Locate every blood parasite and identify its species.
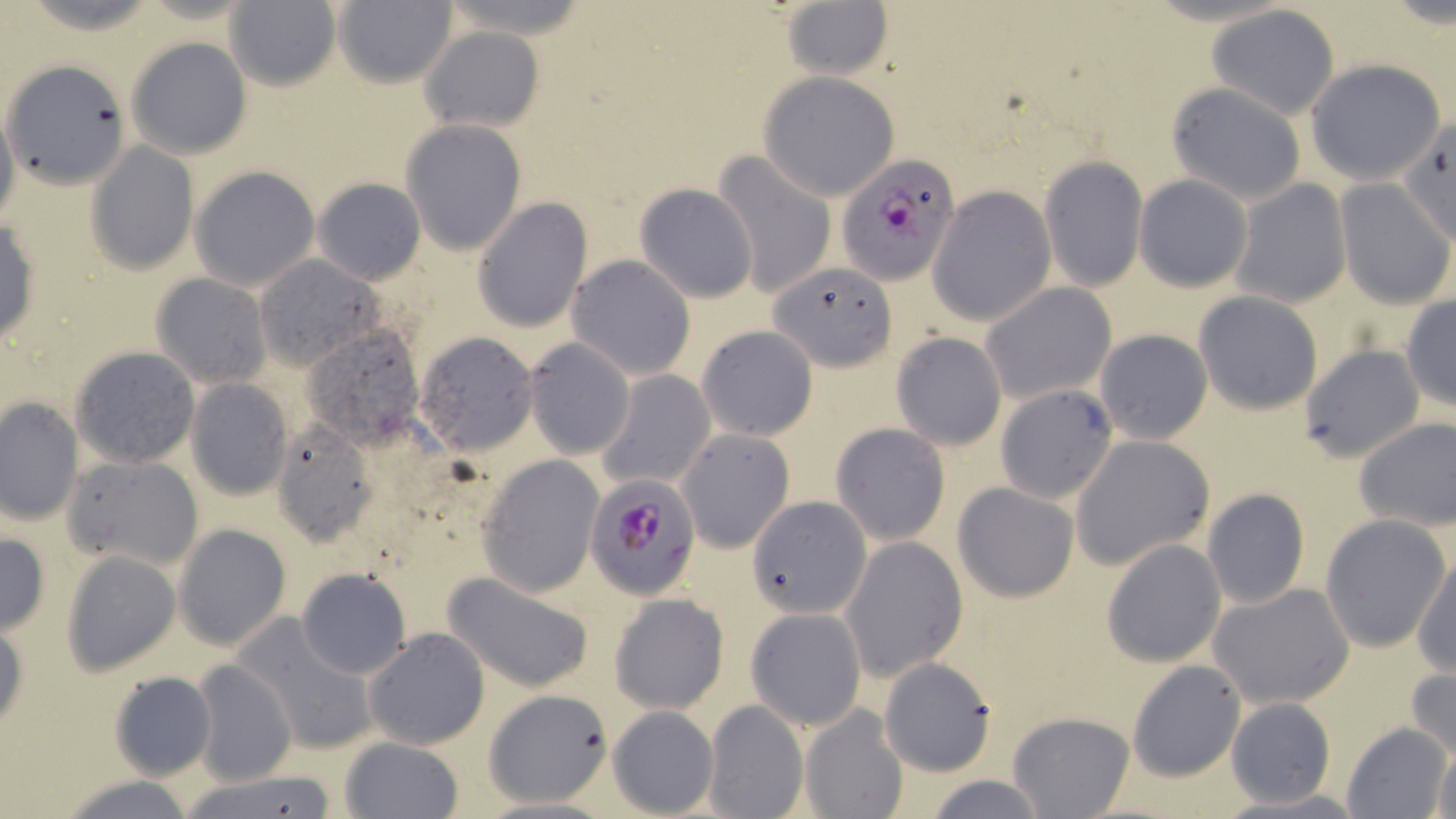
Approximate bounding boxes as [x1, y1, x2, y2] in pixels.
Plasmodium falciparum-infected red blood cells: [837, 153, 961, 285], [587, 473, 703, 598].
No Plasmodium ovale, Plasmodium malariae, Plasmodium vivax, Babesia divergens, or Trypanosoma brucei observed.

Uninfected red blood cell locations: [223, 1, 343, 92], [329, 2, 458, 88], [780, 2, 895, 82], [1206, 6, 1340, 118], [419, 27, 544, 132], [125, 36, 252, 161], [4, 58, 132, 188], [1306, 60, 1445, 184], [757, 72, 899, 201], [1167, 82, 1307, 203], [0, 103, 19, 235], [1398, 118, 1456, 245], [401, 119, 527, 256], [85, 143, 199, 274], [714, 152, 837, 299], [1039, 156, 1147, 290], [189, 164, 320, 290], [1134, 175, 1253, 291], [312, 177, 426, 285], [1230, 180, 1350, 309], [1334, 180, 1454, 307], [634, 183, 758, 304], [927, 185, 1056, 325], [472, 197, 593, 333], [1, 217, 40, 348], [253, 255, 379, 369], [566, 255, 696, 380], [768, 264, 899, 369], [150, 273, 272, 390], [980, 284, 1116, 405], [1194, 292, 1322, 413], [1400, 296, 1455, 414], [301, 324, 428, 447], [696, 325, 818, 441], [1093, 328, 1213, 444], [890, 331, 1007, 451], [414, 332, 540, 454], [524, 337, 635, 459], [1299, 344, 1423, 463], [69, 345, 200, 468], [594, 369, 716, 491], [187, 378, 294, 500], [995, 384, 1119, 503], [0, 396, 84, 527], [1354, 416, 1456, 532], [267, 420, 378, 548], [830, 421, 950, 544], [678, 429, 793, 553], [1070, 435, 1214, 572], [63, 453, 203, 571], [476, 456, 603, 597], [952, 481, 1081, 603], [1201, 487, 1310, 610], [747, 501, 871, 617], [1320, 515, 1452, 652], [174, 524, 292, 651], [0, 530, 51, 634], [840, 536, 966, 682], [1101, 537, 1226, 667], [60, 551, 181, 675], [1412, 553, 1455, 676], [295, 568, 412, 680], [440, 570, 595, 692], [1209, 582, 1354, 708], [610, 594, 729, 714], [746, 607, 866, 731], [0, 617, 28, 738], [235, 617, 379, 756], [363, 627, 491, 749], [878, 656, 997, 775], [190, 658, 297, 786], [1126, 660, 1246, 782], [1406, 667, 1456, 767], [108, 671, 216, 779], [483, 688, 615, 808], [1224, 698, 1337, 807], [701, 699, 809, 819], [800, 703, 909, 819], [607, 705, 720, 817], [1008, 712, 1134, 818], [1343, 722, 1453, 817], [338, 736, 465, 819], [1429, 736, 1456, 819], [173, 771, 344, 819], [55, 773, 201, 818], [916, 775, 1056, 818]. Slide-level diagnosis: Plasmodium falciparum. Image is 1456×819 pixels. May-Grünwald-Giemsa stain. 1000x magnification. Thin blood film. Optical microscopy. One field of a larger specimen.